Locate every leukocyte (white blood cell).
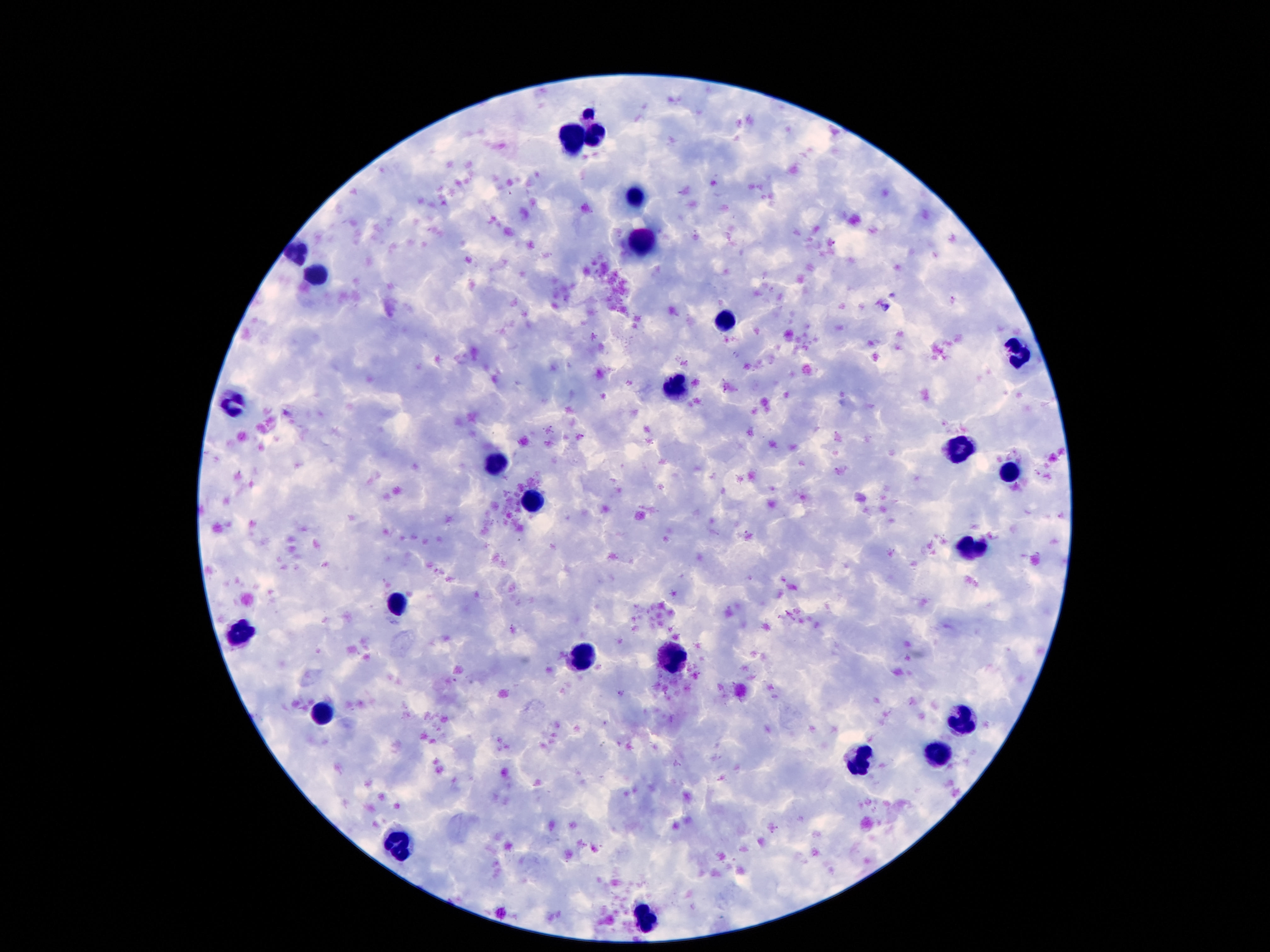
Approximate centers as (x, y) in pixels.
Leukocytes: (595, 135), (572, 139), (636, 199), (644, 243), (298, 252), (316, 276), (724, 322), (1016, 354), (675, 391), (234, 403), (959, 448), (494, 466), (1006, 473), (535, 500), (971, 548), (400, 601), (244, 630), (674, 655), (582, 657), (320, 716), (961, 722), (939, 755), (857, 761), (400, 844), (644, 915).

Giemsa-stained preparation. Thick peripheral-blood smear. Smartphone photograph taken through the microscope eyepiece. 100x magnification. Patient malaria status: not infected. One field from this slide. Image is 1270×952 pixels.